Mark where cells are.
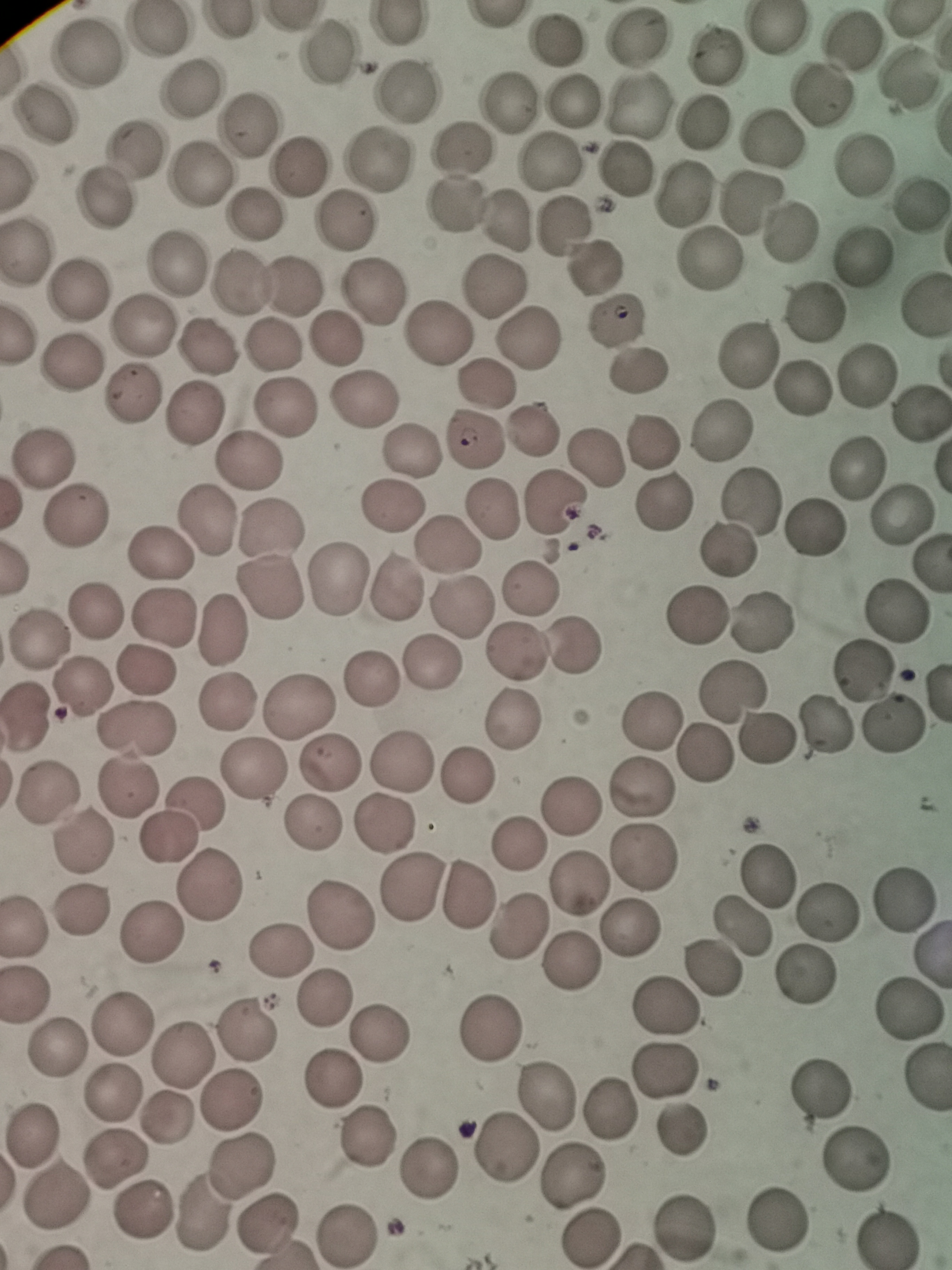
Approximate object centers, in pixels from the top-left corner.
Cells: (x=778, y=28), (x=157, y=31), (x=637, y=34), (x=852, y=40), (x=556, y=41), (x=322, y=54), (x=715, y=54), (x=90, y=55), (x=907, y=78), (x=191, y=88), (x=405, y=92), (x=822, y=95), (x=572, y=99), (x=511, y=101), (x=639, y=105), (x=43, y=116), (x=702, y=122), (x=251, y=126), (x=773, y=139), (x=134, y=147), (x=461, y=147), (x=377, y=161), (x=863, y=162), (x=553, y=163), (x=298, y=167), (x=622, y=171), (x=198, y=177), (x=683, y=193), (x=752, y=199), (x=102, y=202), (x=919, y=203), (x=453, y=204), (x=255, y=215), (x=347, y=220), (x=508, y=221), (x=564, y=224), (x=789, y=231), (x=26, y=250), (x=864, y=255), (x=708, y=259), (x=172, y=266), (x=593, y=268), (x=240, y=286), (x=297, y=287), (x=497, y=287), (x=380, y=288), (x=78, y=291), (x=922, y=306), (x=814, y=311), (x=615, y=323), (x=138, y=325), (x=438, y=333), (x=529, y=333), (x=337, y=341), (x=207, y=346), (x=273, y=346), (x=745, y=353), (x=70, y=366), (x=639, y=369), (x=866, y=376), (x=487, y=385), (x=800, y=387), (x=129, y=394), (x=365, y=395), (x=284, y=407), (x=192, y=416), (x=918, y=416), (x=531, y=428), (x=721, y=429), (x=474, y=441), (x=649, y=442), (x=409, y=449), (x=596, y=456), (x=250, y=460), (x=43, y=461), (x=857, y=466), (x=752, y=500), (x=554, y=504), (x=664, y=504), (x=493, y=505), (x=392, y=506), (x=902, y=513), (x=78, y=517), (x=210, y=519), (x=275, y=521), (x=815, y=528), (x=449, y=544), (x=725, y=549), (x=161, y=551), (x=340, y=580), (x=527, y=583), (x=396, y=587), (x=271, y=591), (x=455, y=608), (x=898, y=608), (x=95, y=609), (x=696, y=615), (x=164, y=616), (x=759, y=622), (x=220, y=630), (x=41, y=640), (x=574, y=641), (x=515, y=651), (x=431, y=664), (x=865, y=669), (x=143, y=670), (x=372, y=675), (x=82, y=687), (x=733, y=689), (x=225, y=701), (x=302, y=703), (x=28, y=719), (x=516, y=720), (x=647, y=721), (x=892, y=722), (x=134, y=726), (x=825, y=730), (x=765, y=739), (x=705, y=752), (x=402, y=757), (x=331, y=763), (x=257, y=769), (x=469, y=773), (x=128, y=785), (x=642, y=788), (x=45, y=792), (x=198, y=801), (x=571, y=805), (x=386, y=823), (x=312, y=824), (x=170, y=835), (x=85, y=839), (x=517, y=844), (x=645, y=856), (x=767, y=874), (x=211, y=879), (x=578, y=884), (x=412, y=886), (x=466, y=896), (x=905, y=897), (x=79, y=909), (x=343, y=912), (x=829, y=912), (x=24, y=926), (x=517, y=927), (x=629, y=927), (x=742, y=928), (x=152, y=932), (x=280, y=951), (x=571, y=961), (x=714, y=970), (x=807, y=977), (x=24, y=993), (x=324, y=998), (x=671, y=1006), (x=910, y=1007), (x=122, y=1027), (x=493, y=1028), (x=246, y=1030), (x=380, y=1034), (x=57, y=1054), (x=179, y=1054), (x=662, y=1070), (x=334, y=1080), (x=819, y=1086), (x=112, y=1091), (x=548, y=1096), (x=231, y=1100), (x=610, y=1110), (x=167, y=1120), (x=680, y=1131), (x=33, y=1135), (x=364, y=1140), (x=506, y=1149), (x=858, y=1152), (x=117, y=1158), (x=241, y=1163), (x=430, y=1168), (x=571, y=1177), (x=57, y=1198), (x=142, y=1211), (x=203, y=1212), (x=773, y=1216), (x=684, y=1224), (x=268, y=1225), (x=884, y=1234), (x=349, y=1236), (x=593, y=1239).

field_of_view: single
stain: Giemsa
capture: smartphone through the microscope eyepiece
image_size: 952×1270 pixels
preparation: thin blood film